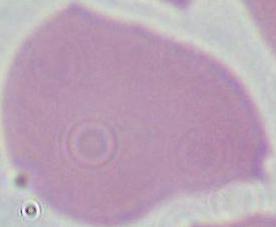

{
  "modality": "micrograph",
  "identification": "red blood cell",
  "magnification": "1000x"
}